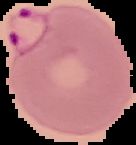
image_type: cell region segmented out of the field of view; surrounding area masked to black
preparation: thin blood film
image_size: 136×145 pixels
malaria_status: parasitized